Identify the parasite.
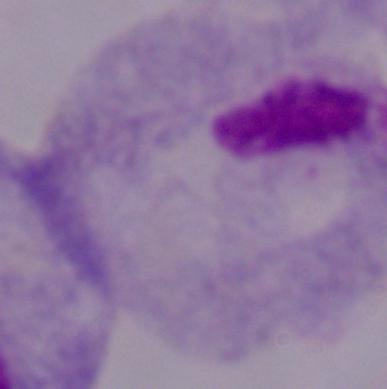

This is a trichomonad.

magnification = 1000x
modality = micrograph